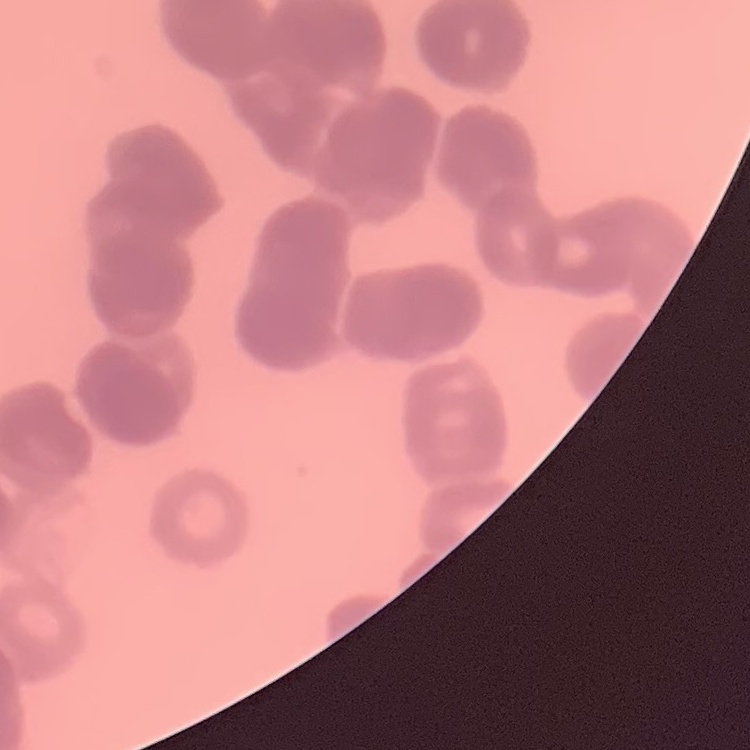
{
  "erythrocyte_morphology": "rouleaux formation",
  "stain": "Field's or Giemsa",
  "image_type": "one tile cut from a larger photomicrograph",
  "preparation": "thin peripheral smear"
}